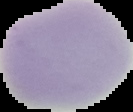 Image is 133×112 pixels. From a thin blood smear. The area outside the segmented cell region is set to black. Malaria status: uninfected.